Classify this cell by malaria status.
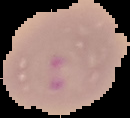
It is parasitized.

{
  "image_type": "cell region segmented out of the field of view; surrounding area masked to black",
  "image_size": "130×118 pixels",
  "preparation": "thin blood film"
}